Classify this cell by malaria status.
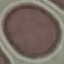

Uninfected.

image type = automatically extracted cell patch, resized to 64 × 64 pixels
stain = Giemsa
preparation = thin smear
capture = smartphone through the microscope eyepiece